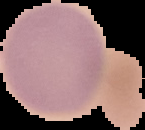
Malaria status: uninfected. From a thin blood smear. The area outside the segmented cell region is set to black. Image is 145×130 pixels.